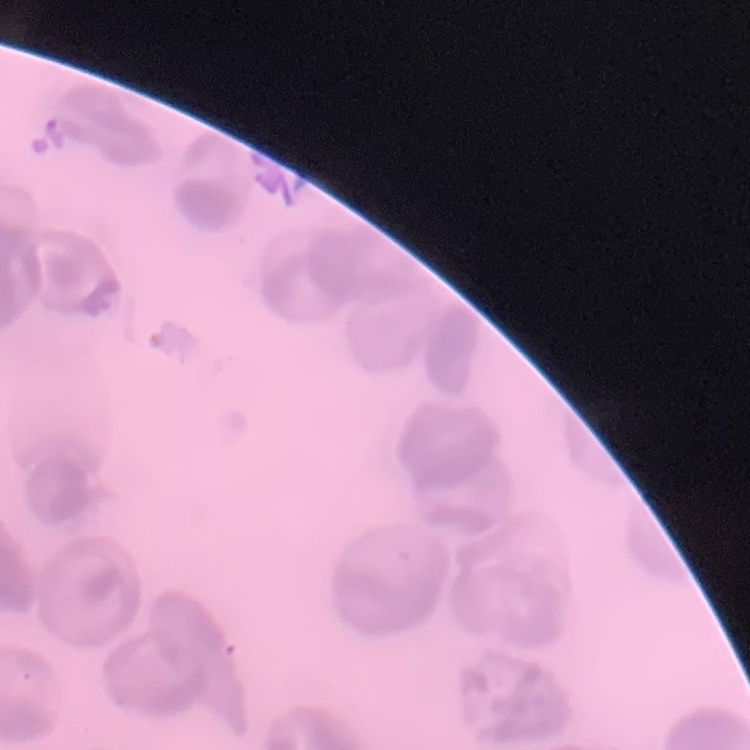
Summary:
  - Erythrocyte morphology: no rouleaux formation
  - Stain: Field's or Giemsa
  - Preparation: thin peripheral smear
  - Image type: one tile cut from a larger photomicrograph